Outline each uninfected red blood cell.
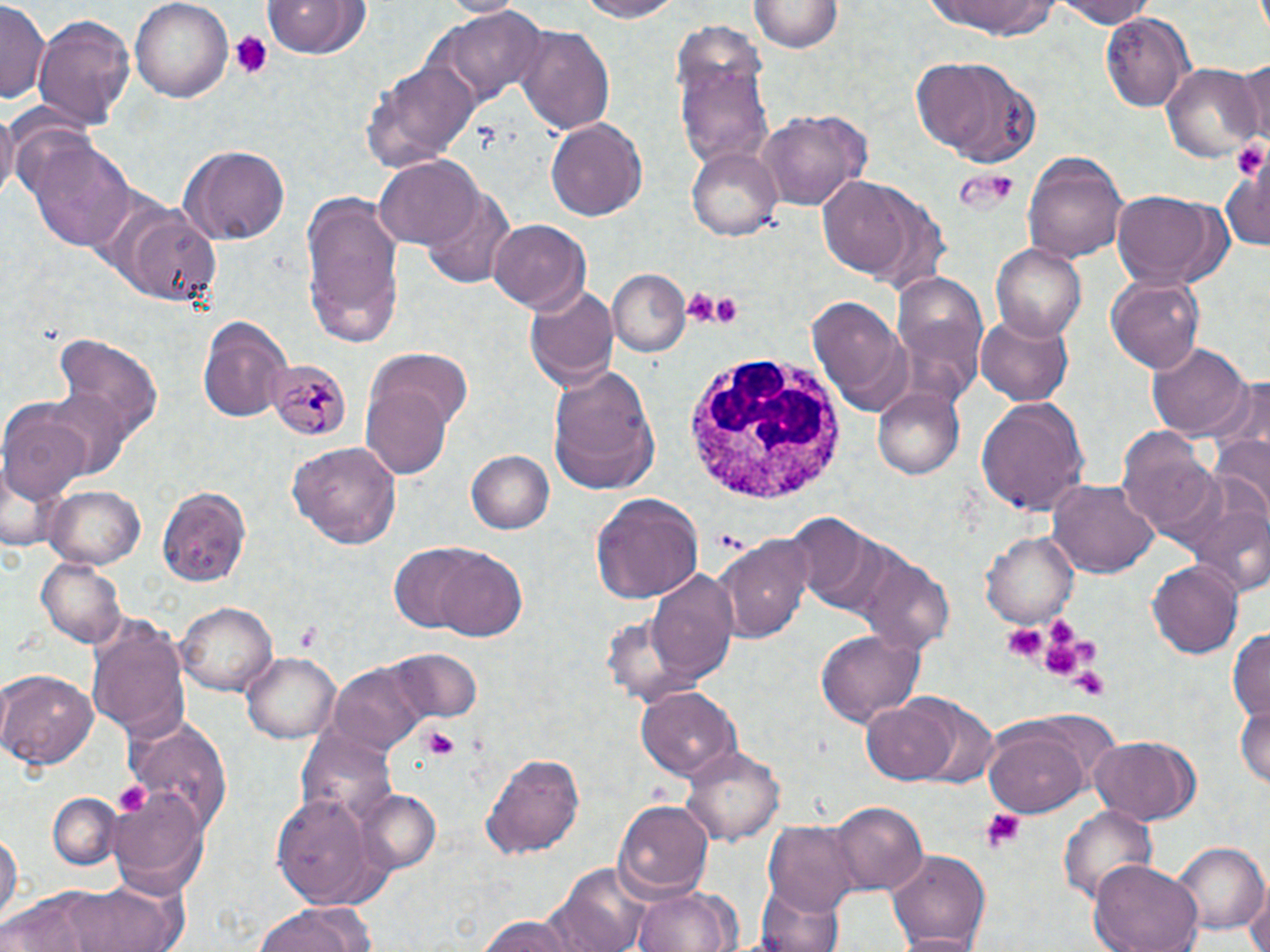

Approximate bounding boxes as (x1,y1)-(x2,y2) corner pairs in pixels.
Uninfected red blood cells: (130,0)-(234,103), (576,0)-(684,20), (1050,0)-(1155,27), (263,1)-(370,58), (436,1)-(529,17), (751,1)-(844,52), (932,1)-(1056,39), (0,2)-(50,105), (432,5)-(549,111), (1100,13)-(1196,111), (31,14)-(135,128), (516,23)-(615,137), (675,51)-(774,172), (913,55)-(1042,168), (361,57)-(479,174), (1235,61)-(1270,145), (1160,63)-(1265,162), (0,102)-(17,204), (757,108)-(871,211), (546,117)-(648,221), (25,137)-(138,253), (177,143)-(290,245), (687,146)-(782,240), (1023,153)-(1129,262), (375,154)-(483,249), (1222,162)-(1268,254), (817,176)-(918,279), (421,186)-(514,287), (300,190)-(407,347), (1112,190)-(1220,288), (102,196)-(221,307), (488,218)-(590,312), (992,244)-(1087,340), (607,270)-(691,357), (1105,275)-(1204,374), (892,278)-(992,401), (525,284)-(619,391), (809,296)-(912,415), (976,313)-(1074,406), (197,315)-(292,422), (54,334)-(164,446), (1147,341)-(1252,440), (364,345)-(473,442), (549,365)-(661,495), (1210,377)-(1270,470), (361,384)-(457,480), (42,385)-(136,478), (872,387)-(965,481), (0,397)-(92,503), (977,397)-(1090,516), (1116,428)-(1218,540), (1209,435)-(1270,531), (287,441)-(402,548), (466,450)-(555,534), (1048,479)-(1158,579), (42,485)-(143,569), (156,486)-(252,587), (589,493)-(705,604), (1188,499)-(1269,600), (784,513)-(890,616), (979,531)-(1078,629), (716,536)-(812,643), (421,545)-(528,641), (856,550)-(956,656), (37,558)-(128,648), (1148,560)-(1244,658), (644,568)-(735,683), (175,602)-(279,695), (599,608)-(703,706), (87,616)-(191,741), (1228,628)-(1270,722), (813,629)-(924,728), (386,646)-(485,726), (241,652)-(342,742), (327,662)-(426,755), (0,668)-(98,770), (0,674)-(12,750), (636,685)-(741,781), (903,694)-(1000,789), (862,697)-(962,785), (1235,701)-(1269,790), (124,713)-(231,833), (983,719)-(1093,818), (295,730)-(397,827), (1090,734)-(1201,826), (680,744)-(786,845), (481,751)-(586,860), (355,788)-(441,875), (107,790)-(209,895), (47,791)-(122,871), (270,791)-(387,910), (612,800)-(713,898), (828,800)-(927,895), (1057,804)-(1158,907), (764,821)-(862,913), (0,828)-(21,926), (1175,844)-(1268,935), (884,848)-(991,950), (1087,859)-(1203,952), (547,863)-(652,952), (70,877)-(190,952), (1246,881)-(1270,952), (753,884)-(846,952), (2,888)-(111,951), (632,888)-(739,952), (253,902)-(378,952), (475,913)-(578,951), (892,933)-(984,951).

Summary:
  - Plasmodium malariae-infected red blood cell locations: (267,359)-(352,443)
  - Platelet locations: (228,31)-(273,79), (1232,141)-(1269,178), (962,169)-(1023,211), (682,288)-(722,326), (709,291)-(742,326), (1002,621)-(1048,664), (293,623)-(319,651), (1035,625)-(1092,674), (1071,666)-(1111,701), (421,726)-(461,761), (112,781)-(151,818), (980,808)-(1026,852)
  - White blood cell locations: (682,354)-(847,504)
  - Slide-level diagnosis: Plasmodium malariae
  - Preparation: thin blood film
  - Modality: light microscopy
  - Field of view: single
  - Image size: 1270×952 pixels
  - Stain: May-Grünwald-Giemsa
  - Magnification: 1000x